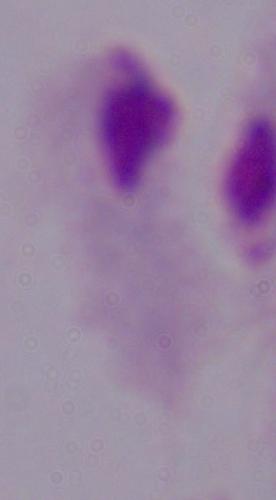

Summary:
  - Modality: photomicrograph
  - Magnification: 1000x
  - Identification: trichomonad